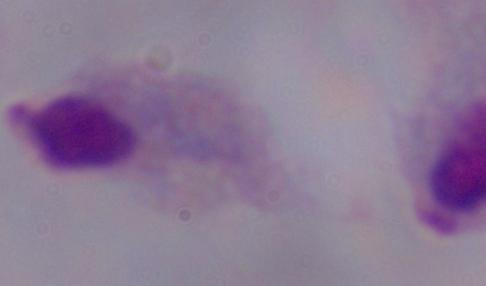

magnification = 1000x
identification = trichomonad
modality = photomicrograph